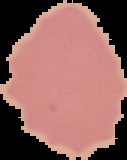

Segmented cell region on a black background. From a thin blood smear. Image is 127×160 pixels. Result: no Plasmodium parasites seen.